Evaluate for malaria.
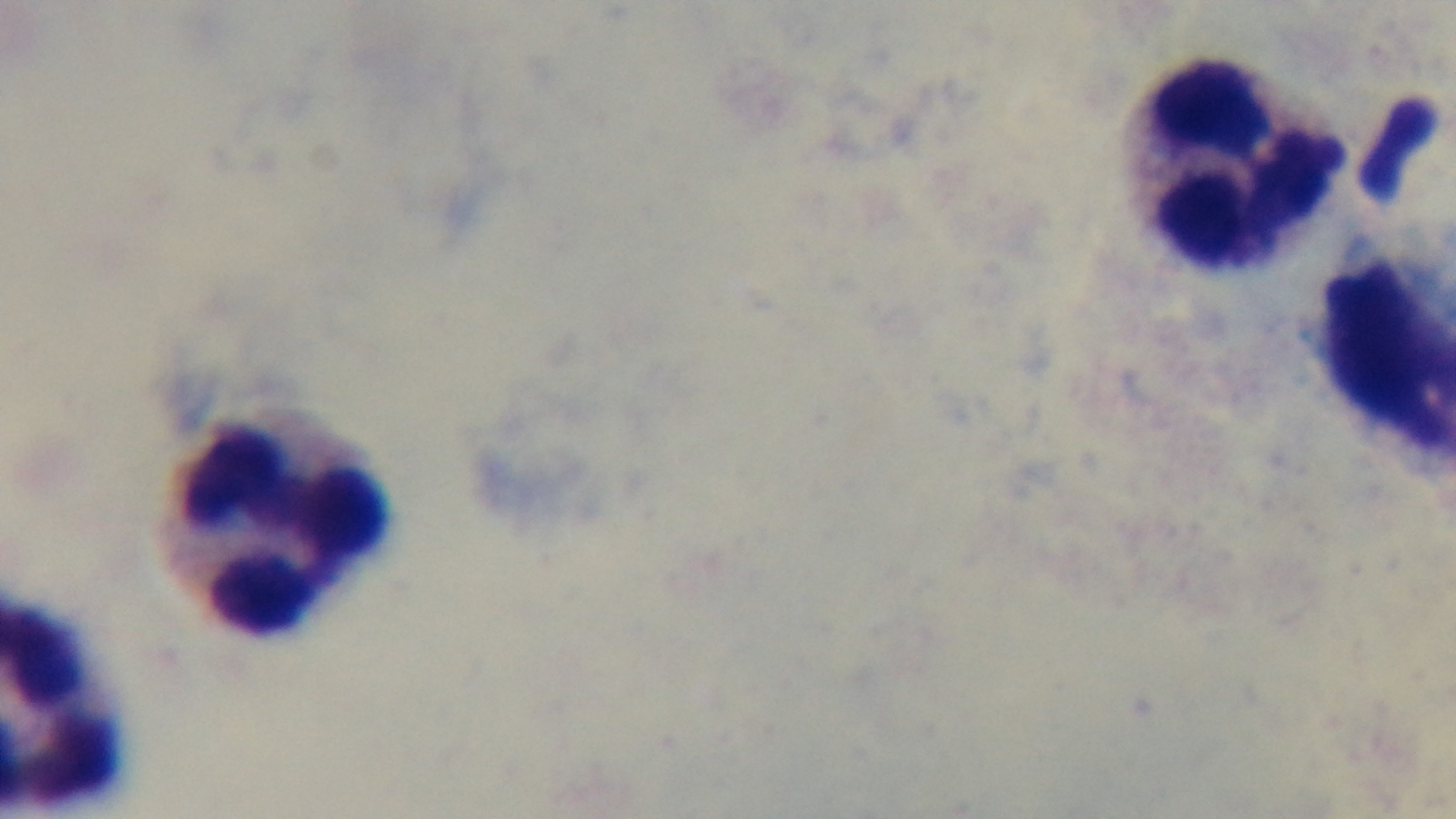

Uninfected.

Summary:
  - Field of view: one from the slide
  - Stain: Giemsa
  - Objective: 100x oil immersion
  - Capture: mounted 4K digital camera
  - Preparation: thick smear
  - Modality: light microscopy